Classify this cell by malaria status.
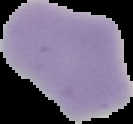
It is uninfected.

From a thin blood film. Image is 133×124 pixels. Cell region segmented out of the field of view; the surrounding area is masked to black.